Report the malaria status of this cell.
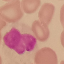
Uninfected.

Summary:
  - Stain: Giemsa
  - Image type: cell patch, automatically extracted from a larger field of view and resized to 64 × 64 pixels
  - Capture: smartphone camera at the microscope eyepiece
  - Preparation: thin blood smear